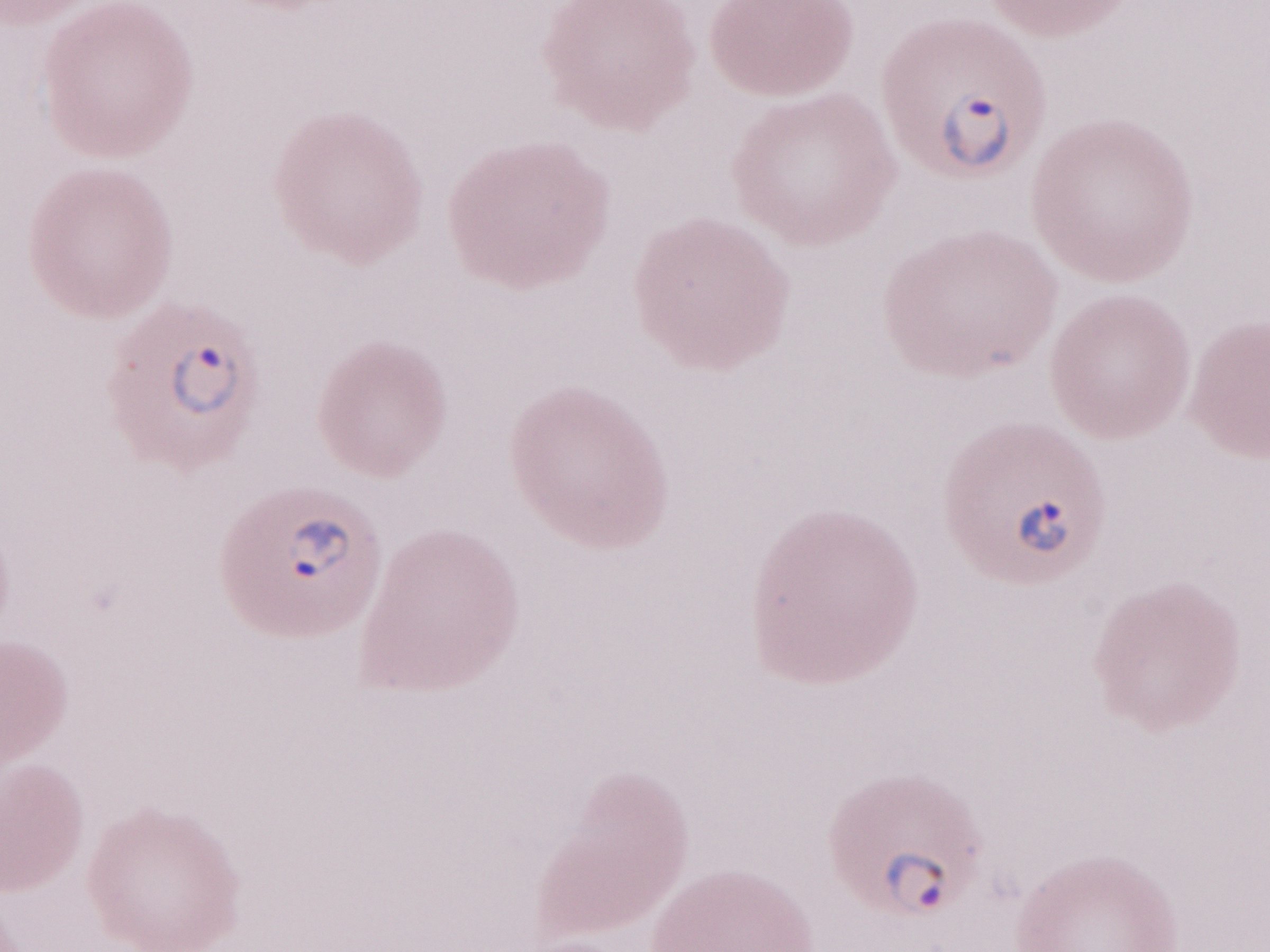

Olympus BX43 microscope and DP73 digital camera. Thin blood smear. Image is 1270×952 pixels. May-Grünwald-Giemsa-stained preparation. One field of this slide. 1,000x magnification. Patient diagnosis: malaria infection.